Assess this cell for malaria.
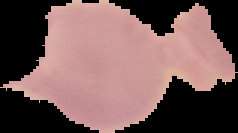
Uninfected.

From a thin blood film. Image is 238×133 pixels. Segmented cell region on a black background.